Assess this cell for malaria.
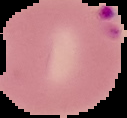

Parasitized.

image type = segmented cell region with the area outside set to black
preparation = thin blood film
image size = 127×118 pixels